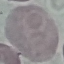
result = no malaria parasites seen
capture = smartphone through the microscope eyepiece
preparation = thin blood smear
image type = automatically extracted cell patch, resized to 64 × 64 pixels
stain = Giemsa